Identify the parasite.
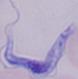
This is a trypanosome.

{
  "magnification": "1000x",
  "modality": "micrograph"
}